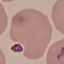
Malaria status: uninfected. Giemsa-stained preparation. Automatically extracted cell patch, resized to 64 × 64 pixels. Thin smear of blood. Acquired by smartphone through the microscope eyepiece.